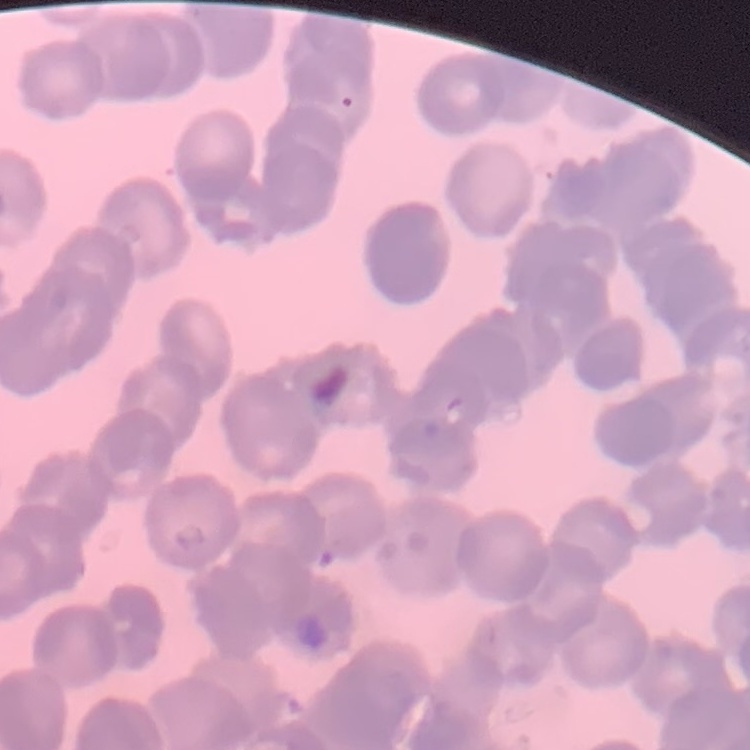

{
  "erythrocyte_morphology": "rouleaux formation",
  "preparation": "thin peripheral smear",
  "stain": "Field's or Giemsa",
  "image_type": "one tile cut from a larger photomicrograph"
}